Identify the blood parasite species.
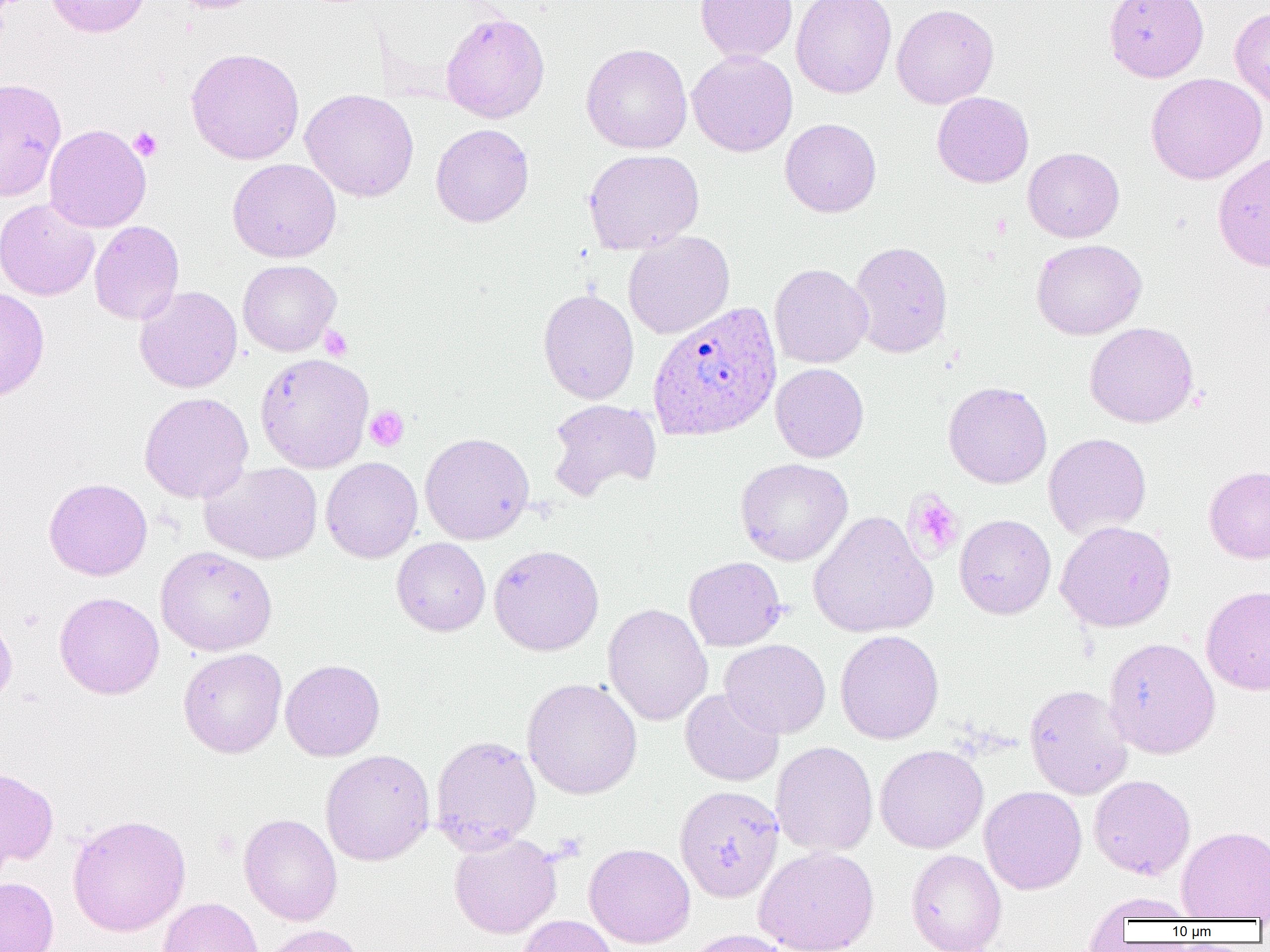

Plasmodium ovale.

Approximate bounding boxes as (x1, y1, x2, y2) in pixels. Plasmodium ovale-infected red blood cell locations: (647, 301, 782, 441). Uninfected red blood cell locations: (45, 0, 150, 38), (170, 0, 266, 13), (695, 0, 798, 62), (791, 0, 897, 98), (1104, 0, 1208, 82), (891, 3, 999, 109), (1229, 7, 1270, 109), (440, 11, 550, 123), (581, 43, 693, 153), (185, 47, 305, 164), (686, 50, 798, 157), (1145, 72, 1267, 184), (0, 78, 66, 201), (300, 89, 419, 202), (932, 91, 1034, 188), (780, 118, 881, 217), (44, 124, 151, 233), (430, 124, 534, 227), (1023, 147, 1124, 243), (583, 149, 704, 255), (1212, 152, 1270, 273), (227, 158, 342, 263), (0, 198, 100, 301), (88, 220, 185, 325), (623, 231, 735, 339), (1032, 238, 1147, 340), (849, 240, 953, 358), (237, 259, 342, 356), (769, 263, 872, 368), (134, 285, 242, 393), (0, 287, 50, 402), (538, 288, 639, 404), (1084, 322, 1199, 428), (255, 353, 374, 473), (770, 363, 869, 462), (943, 381, 1052, 489), (139, 392, 253, 503), (546, 399, 662, 500), (420, 432, 534, 544), (1043, 432, 1152, 540), (321, 457, 422, 563), (735, 458, 853, 566), (200, 461, 322, 564), (1203, 465, 1270, 564), (43, 477, 153, 580), (807, 510, 938, 639), (954, 514, 1056, 619), (1055, 521, 1176, 632), (391, 538, 491, 636), (489, 544, 604, 656), (156, 545, 277, 656), (684, 556, 787, 652), (1201, 584, 1270, 695), (54, 592, 164, 699), (603, 603, 712, 726), (0, 609, 17, 709), (835, 630, 944, 744), (1103, 636, 1220, 759), (720, 639, 831, 738), (178, 648, 287, 758), (280, 659, 385, 761), (521, 678, 643, 800), (1024, 684, 1133, 799), (680, 688, 784, 786), (430, 735, 541, 853), (770, 741, 878, 857), (875, 744, 988, 854), (320, 749, 435, 866), (0, 765, 59, 869), (1089, 774, 1195, 880), (675, 785, 784, 902), (979, 786, 1087, 895), (66, 813, 191, 937), (239, 813, 342, 926), (1177, 826, 1270, 920), (448, 832, 562, 938), (583, 842, 695, 948), (753, 845, 879, 952), (906, 849, 1006, 952), (0, 877, 59, 952), (1085, 892, 1198, 923), (157, 896, 263, 952), (515, 914, 618, 952), (258, 924, 367, 952), (682, 929, 794, 952). Platelet locations: (128, 127, 163, 161), (320, 326, 352, 361), (365, 406, 409, 451), (905, 491, 964, 560). Image is 1270×952 pixels. One field of a larger specimen. Thin blood film. 1000x magnification. Optical microscopy.